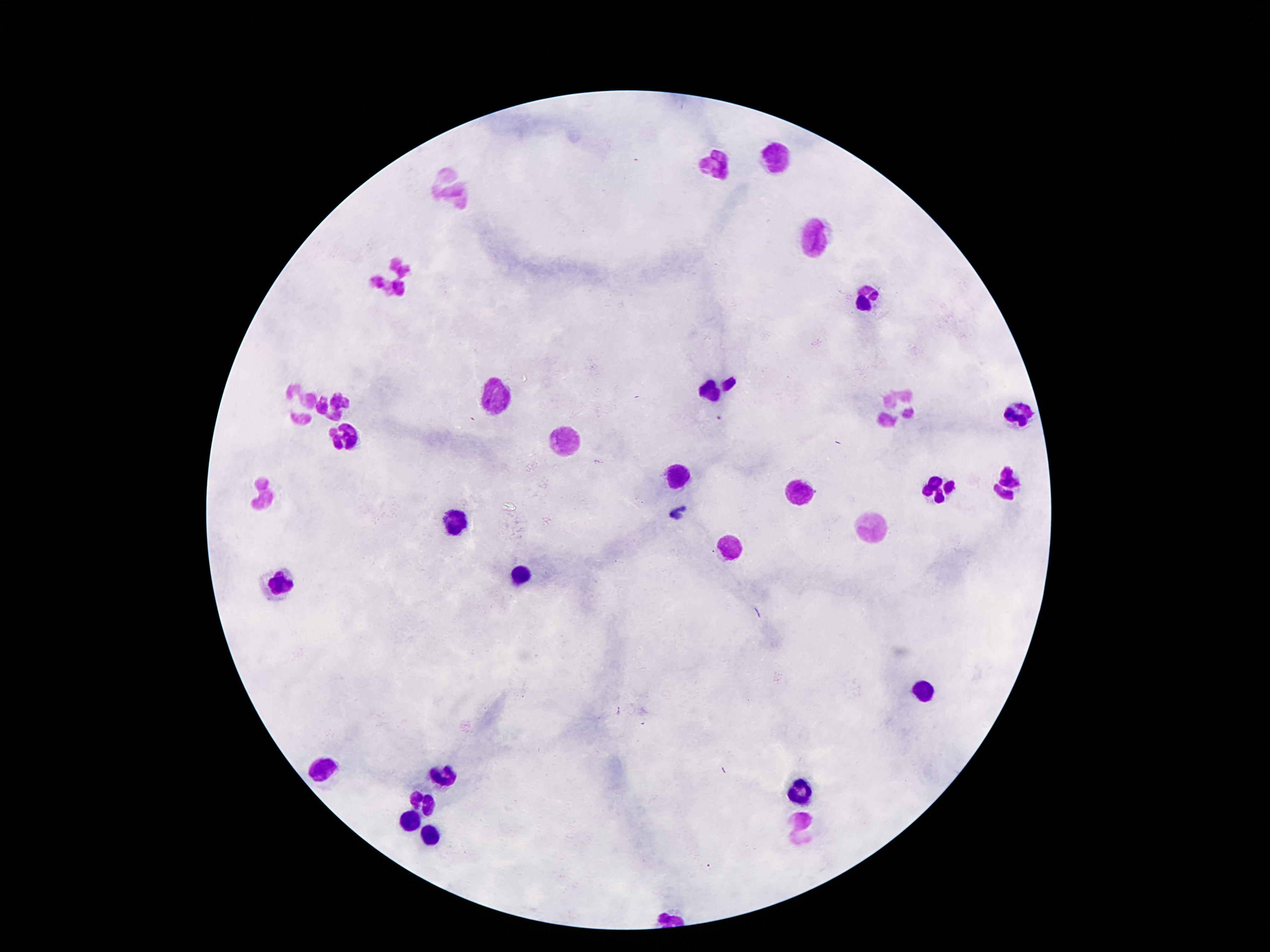

Approximate centers as [x, y] in pixels.
Summary:
  - Leukocyte locations: [777, 156], [716, 164], [452, 185], [814, 236], [390, 279], [868, 297], [720, 386], [497, 397], [302, 402], [331, 406], [892, 406], [1015, 414], [562, 434], [345, 437], [679, 476], [1007, 483], [937, 488], [800, 490], [261, 498], [454, 519], [872, 527], [730, 547], [521, 569], [281, 582], [925, 688], [318, 768], [437, 778], [800, 787], [423, 799], [411, 821], [800, 828], [429, 834]
  - Patient malaria status: not infected
  - Image size: 1270×952 pixels
  - Magnification: 100x
  - Stain: Giemsa
  - Capture: smartphone camera through the microscope eyepiece
  - Preparation: thick blood film
  - Field of view: single